Locate every leukocyte (white blood cell).
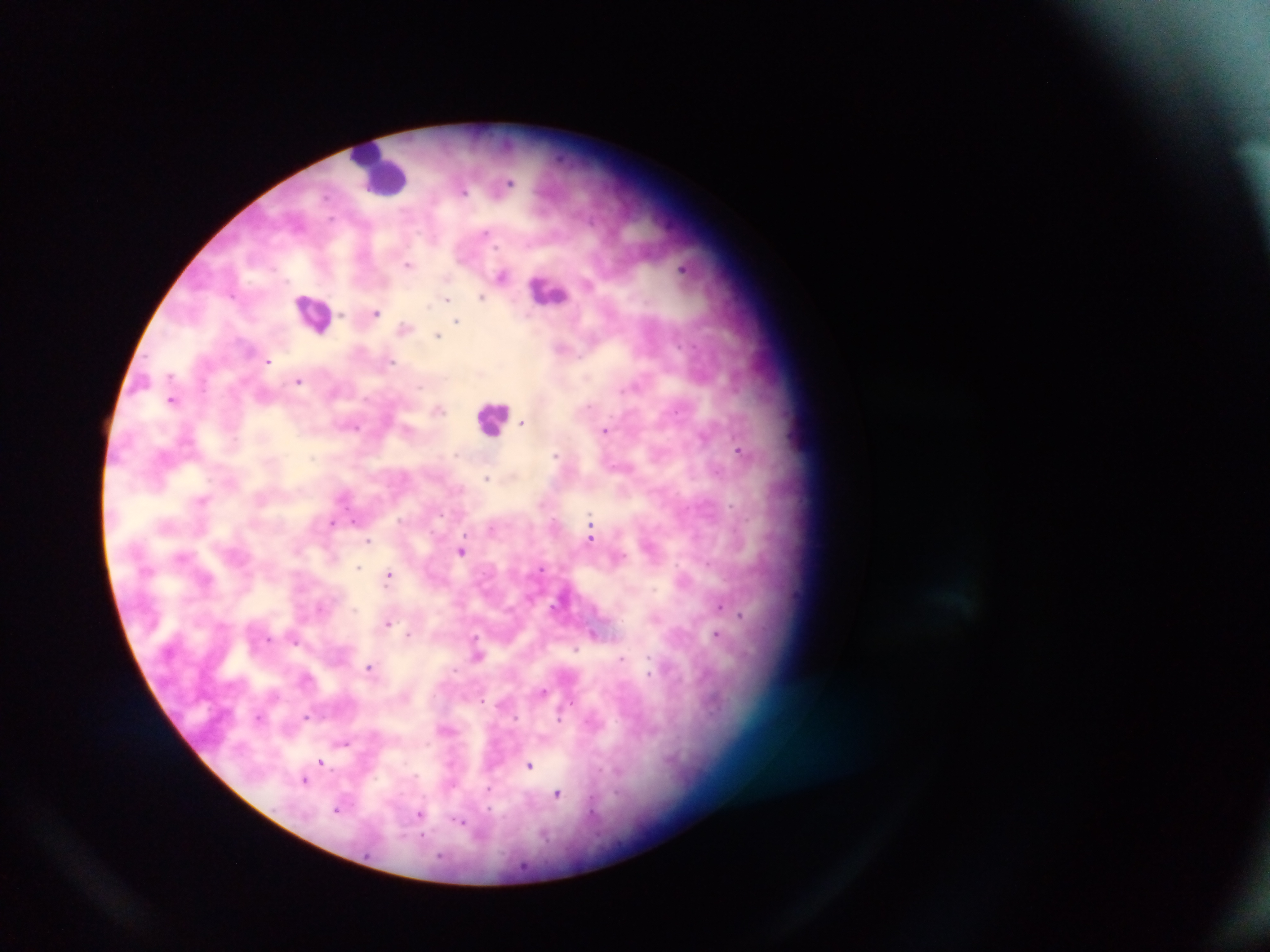

Approximate centers as [x, y] in pixels.
Leukocytes: [379, 170], [548, 290], [314, 313], [492, 418].

Malaria parasite locations: [507, 184], [463, 190], [409, 264], [684, 268], [502, 275], [482, 295], [447, 298], [375, 312], [457, 320], [405, 327], [438, 334], [562, 347], [268, 360], [298, 381], [174, 398], [438, 409], [523, 422], [606, 430], [741, 450], [488, 478], [204, 499], [331, 522], [592, 525], [492, 527], [591, 533], [368, 540], [462, 550], [359, 568], [390, 575], [720, 605], [741, 615], [656, 617], [388, 622], [409, 634], [593, 634], [718, 635], [478, 654], [370, 667], [543, 691], [259, 717], [305, 717], [446, 729], [344, 742], [322, 762], [529, 765], [305, 779], [489, 790], [558, 793], [337, 809], [421, 814], [462, 821]. Image is 1270×952 pixels. One field of view. Thick blood film. Photographed through a microscope with a mobile-phone camera. Sample from Ghana.